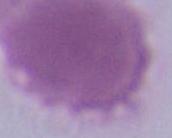
{
  "modality": "photomicrograph",
  "identification": "red blood cell",
  "magnification": "1000x"
}